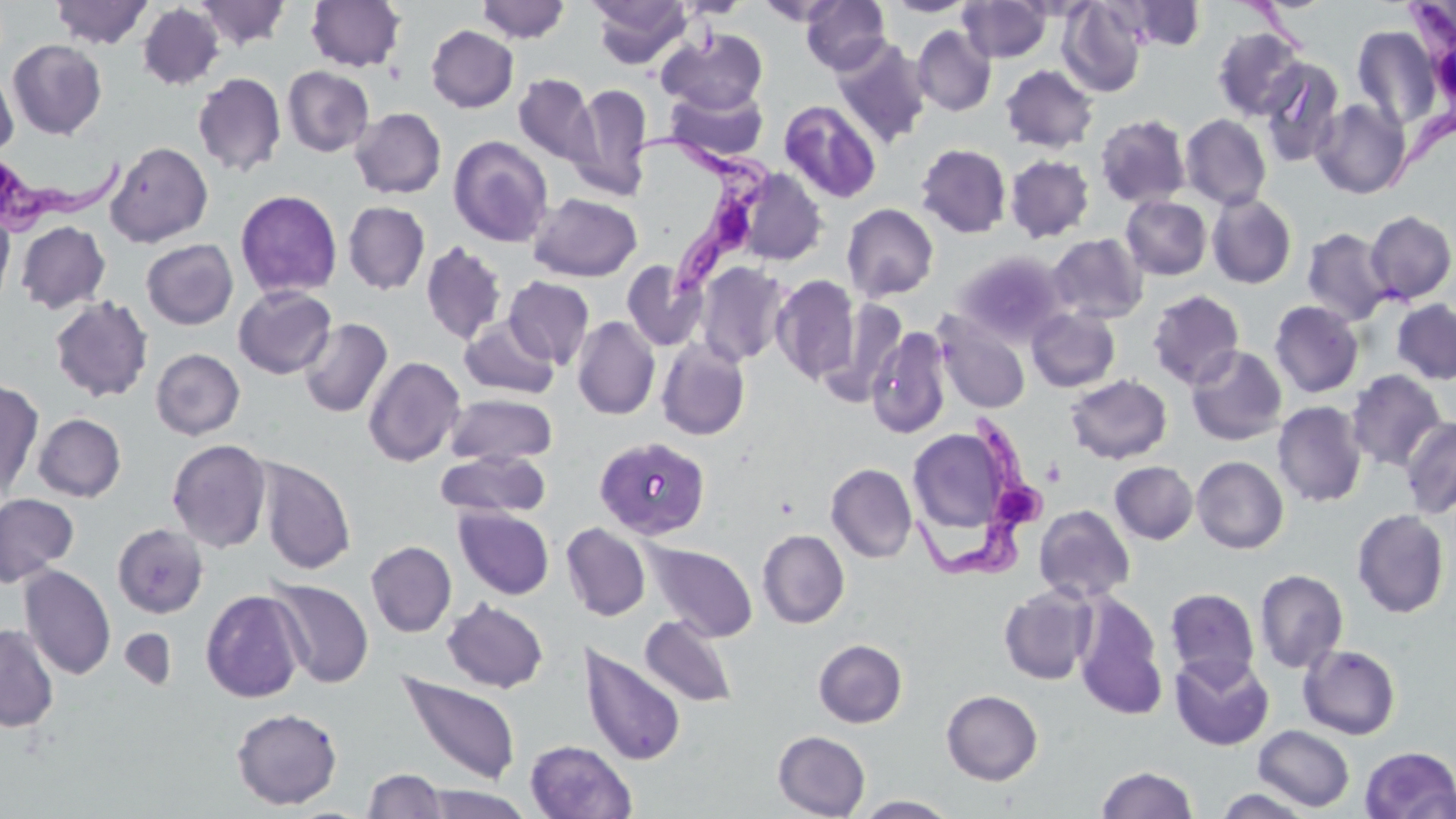
Summary:
  - Coordinate format: approximate bounding boxes as [x1, y1, x2, y2] in pixels
  - Trypanosoma brucei locations: [1384, 0, 1456, 196], [627, 132, 774, 304], [1, 151, 131, 239], [914, 412, 1048, 581]
  - Uninfected red blood cell locations: [50, 0, 153, 49], [194, 0, 291, 51], [305, 0, 406, 72], [477, 0, 569, 43], [590, 0, 691, 68], [675, 0, 752, 18], [756, 0, 848, 27], [801, 0, 890, 74], [1123, 0, 1207, 50], [882, 1, 978, 17], [958, 1, 1051, 62], [1058, 1, 1148, 97], [137, 3, 225, 90], [426, 25, 518, 113], [912, 25, 996, 116], [1352, 26, 1441, 131], [1212, 27, 1307, 121], [657, 28, 768, 114], [831, 37, 931, 147], [8, 39, 107, 139], [1259, 59, 1344, 168], [0, 64, 18, 158], [1000, 64, 1098, 153], [282, 66, 374, 157], [193, 72, 287, 177], [513, 73, 598, 166], [567, 83, 652, 201], [664, 85, 768, 164], [1311, 99, 1411, 199], [779, 100, 881, 204], [350, 107, 446, 198], [1095, 114, 1191, 208], [1181, 114, 1271, 210], [448, 135, 553, 247], [105, 141, 213, 247], [916, 143, 1012, 238], [1005, 155, 1094, 243], [735, 168, 828, 266], [235, 189, 342, 299], [529, 193, 643, 282], [1207, 193, 1297, 289], [1121, 196, 1212, 280], [343, 202, 430, 295], [842, 203, 938, 302], [0, 206, 15, 314], [1365, 210, 1456, 304], [15, 221, 110, 313], [1302, 227, 1393, 325], [1047, 233, 1147, 323], [141, 239, 238, 330], [421, 242, 507, 345], [955, 250, 1068, 345], [621, 260, 706, 350], [694, 262, 791, 367], [771, 275, 860, 385], [503, 276, 594, 369], [233, 285, 336, 379], [1147, 290, 1245, 389], [49, 296, 154, 402], [819, 298, 908, 408], [1390, 299, 1456, 385], [1269, 300, 1364, 397], [1027, 308, 1120, 392], [934, 312, 1030, 414], [572, 316, 660, 420], [298, 318, 393, 418], [459, 318, 559, 399], [866, 327, 952, 439], [656, 338, 751, 441], [1186, 346, 1287, 445], [151, 348, 245, 440], [363, 356, 466, 467], [1346, 370, 1447, 472], [1065, 374, 1172, 464], [0, 378, 44, 498], [445, 394, 557, 467], [1273, 401, 1367, 507], [32, 413, 127, 502], [1400, 415, 1456, 518], [906, 425, 1021, 542], [593, 436, 710, 539], [167, 438, 271, 552], [436, 450, 549, 519], [1191, 456, 1289, 554], [258, 458, 356, 575], [1110, 461, 1198, 544], [825, 463, 917, 563], [0, 493, 79, 587], [1033, 505, 1135, 604], [454, 506, 554, 600], [1352, 509, 1451, 618], [112, 523, 208, 618], [561, 523, 650, 621], [757, 529, 849, 628], [366, 541, 456, 637], [644, 541, 758, 642], [20, 565, 116, 680], [1254, 569, 1348, 674], [266, 577, 374, 689], [998, 585, 1098, 685], [1165, 588, 1260, 685], [200, 589, 305, 703], [1072, 591, 1169, 721], [442, 599, 549, 693], [640, 615, 737, 708], [0, 624, 59, 732], [120, 627, 177, 691], [813, 639, 907, 728], [579, 643, 686, 765], [1299, 644, 1401, 740], [1170, 653, 1274, 750], [399, 673, 521, 786], [941, 689, 1043, 786], [231, 707, 343, 810], [1253, 725, 1355, 812], [773, 731, 870, 818], [525, 740, 637, 819], [1359, 746, 1456, 819], [1095, 765, 1200, 818], [363, 768, 448, 819], [417, 785, 535, 819], [1213, 788, 1316, 818], [854, 795, 960, 818]
  - Slide-level diagnosis: Trypanosoma brucei
  - Preparation: thin blood smear
  - Modality: light microscopy
  - Magnification: 1000x
  - Field of view: one of a larger specimen
  - Image size: 1456×819 pixels
  - Stain: May-Grünwald-Giemsa